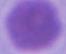

Summary:
  - Identification: erythrocyte
  - Modality: micrograph
  - Magnification: 1000x